Locate every blood parasite and identify its species.
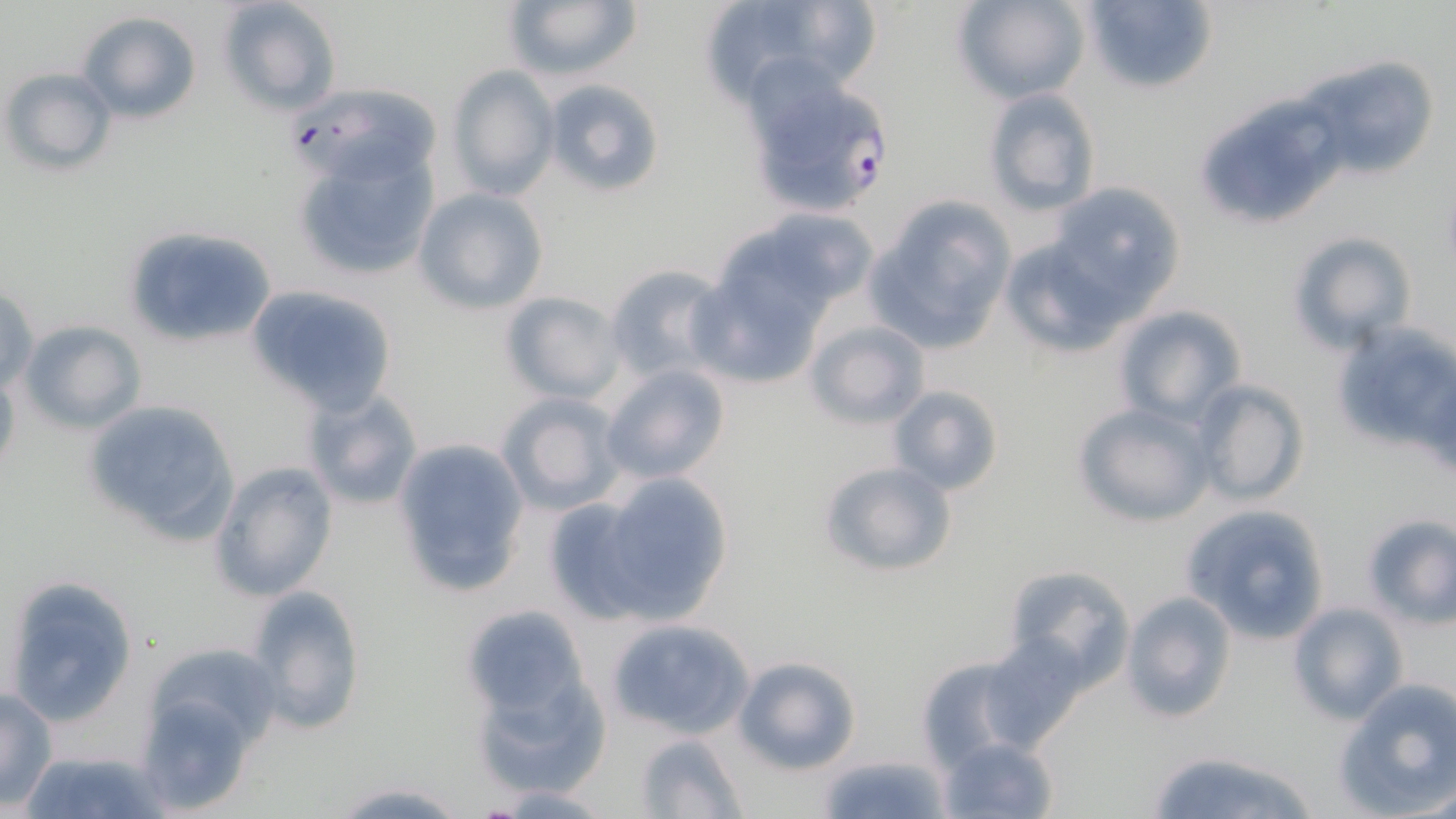
Approximate bounding boxes as (x1, y1, x2, y2) in pixels.
Plasmodium falciparum-infected red blood cells: (743, 71, 896, 220).
No Plasmodium ovale, Plasmodium malariae, Plasmodium vivax, Babesia divergens, or Trypanosoma brucei observed.

Summary:
  - Uninfected red blood cell locations: (218, 0, 342, 115), (502, 0, 644, 86), (762, 0, 896, 91), (951, 0, 1091, 104), (1081, 0, 1219, 95), (706, 1, 822, 114), (74, 11, 202, 124), (1302, 60, 1439, 182), (444, 66, 559, 201), (4, 67, 116, 176), (543, 77, 664, 198), (288, 83, 442, 189), (983, 89, 1102, 216), (1206, 100, 1348, 222), (292, 142, 438, 280), (1044, 181, 1187, 314), (411, 188, 549, 314), (862, 200, 1012, 352), (748, 209, 880, 311), (125, 224, 280, 347), (1000, 230, 1145, 357), (1287, 230, 1417, 353), (606, 264, 728, 380), (686, 270, 827, 389), (245, 284, 398, 416), (0, 285, 39, 397), (501, 291, 627, 404), (1114, 305, 1246, 426), (1327, 318, 1456, 453), (18, 319, 146, 433), (803, 320, 930, 428), (600, 363, 732, 485), (0, 372, 21, 482), (1191, 380, 1309, 507), (887, 385, 1003, 497), (300, 387, 424, 512), (497, 392, 625, 515), (80, 398, 242, 547), (1072, 402, 1215, 528), (392, 437, 530, 598), (816, 460, 958, 580), (210, 461, 337, 602), (600, 474, 735, 621), (541, 494, 662, 626), (1181, 504, 1330, 644), (1358, 514, 1456, 626), (1002, 565, 1136, 689), (3, 573, 138, 729), (244, 585, 367, 737), (1120, 590, 1235, 723), (1286, 601, 1408, 725), (459, 605, 589, 721), (605, 617, 754, 740), (978, 632, 1090, 748), (144, 641, 283, 751), (912, 650, 1043, 770), (730, 655, 860, 774), (467, 658, 610, 798), (1335, 680, 1456, 814), (1, 687, 56, 809), (135, 692, 262, 813), (633, 732, 749, 817), (939, 735, 1058, 818), (21, 748, 167, 819), (1142, 750, 1322, 819), (822, 753, 946, 819), (326, 781, 474, 818), (487, 784, 620, 816), (1404, 784, 1456, 818)
  - Slide-level diagnosis: Plasmodium falciparum
  - Modality: optical microscopy
  - Magnification: 1000x
  - Image size: 1456×819 pixels
  - Field of view: single
  - Preparation: thin blood film
  - Stain: May-Grünwald-Giemsa